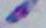

Summary:
  - Identification: Toxoplasma gondii
  - Modality: micrograph
  - Magnification: 1000x